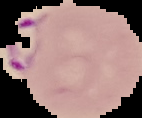

Summary:
  - Image type: segmented cell region with the area outside set to black
  - Malaria status: parasitized
  - Image size: 142×118 pixels
  - Preparation: thin blood smear